Name the parasite shown.
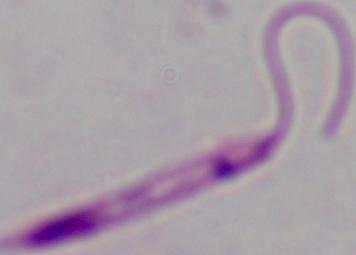

This is Leishmania.

Micrograph. 1000x magnification.